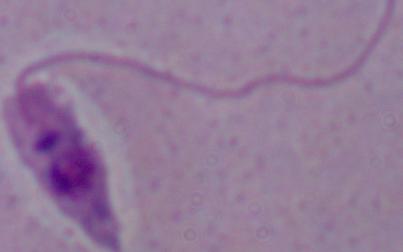

{
  "magnification": "1000x",
  "modality": "micrograph",
  "identification": "Leishmania"
}